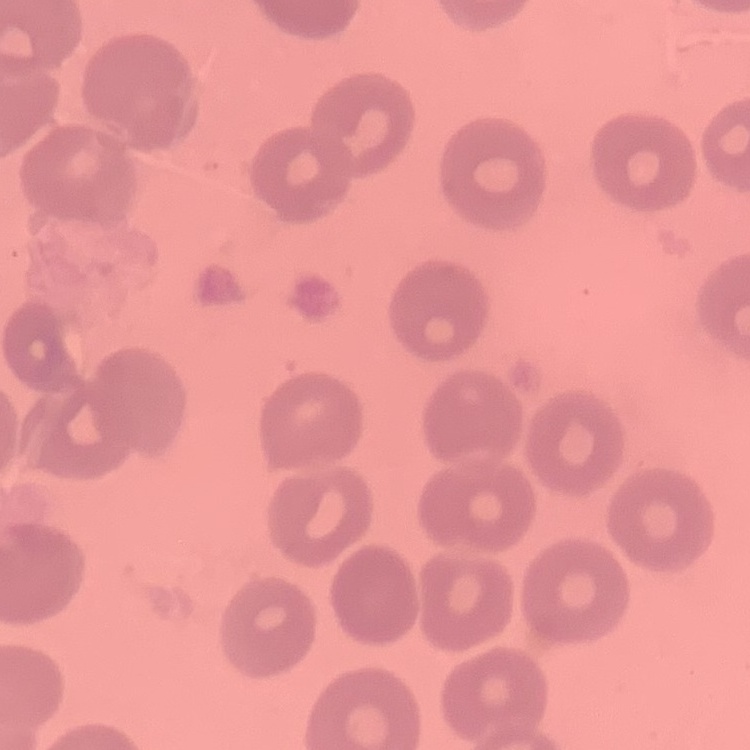
erythrocyte morphology = no rouleaux formation
preparation = thin peripheral smear
image type = square crop of a larger photomicrograph
stain = Field's or Giemsa